Assess the morphology of the erythrocytes.
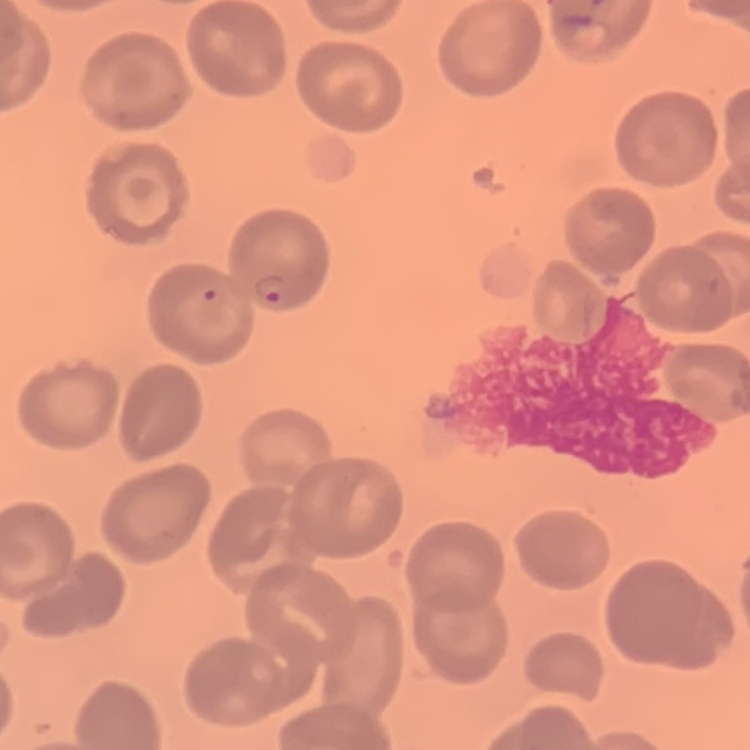
They show no rouleaux formation.

Summary:
  - Stain: Field's or Giemsa
  - Image type: one tile cut from a larger photomicrograph
  - Preparation: thin blood film